Report the malaria status of this cell.
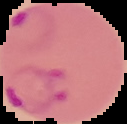

It is parasitized.

Image is 127×124 pixels. From a thin blood smear. Segmented cell region on a black background.